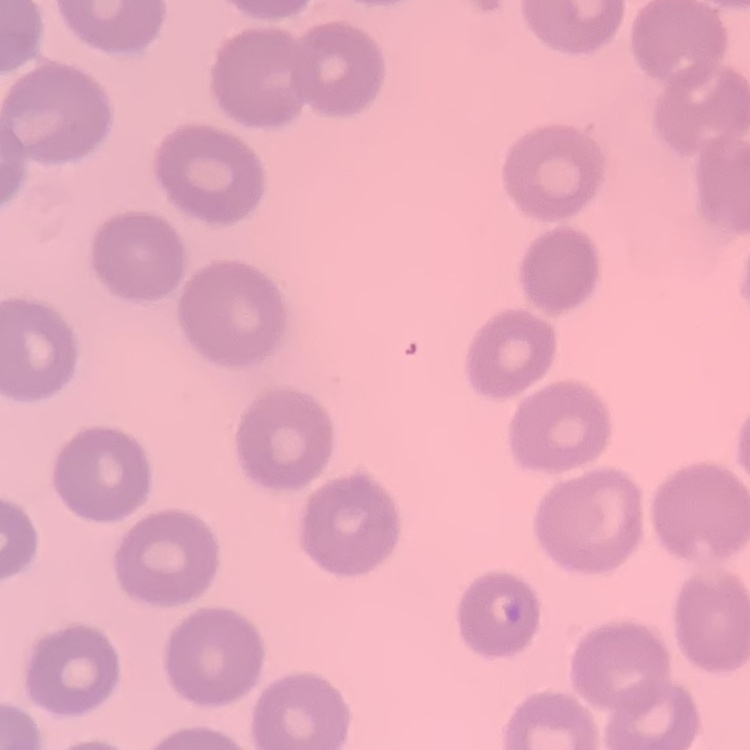

erythrocyte morphology = no rouleaux formation
stain = Field's or Giemsa
image type = one tile cut from a larger photomicrograph
preparation = thin peripheral smear